Identify the preparation type.
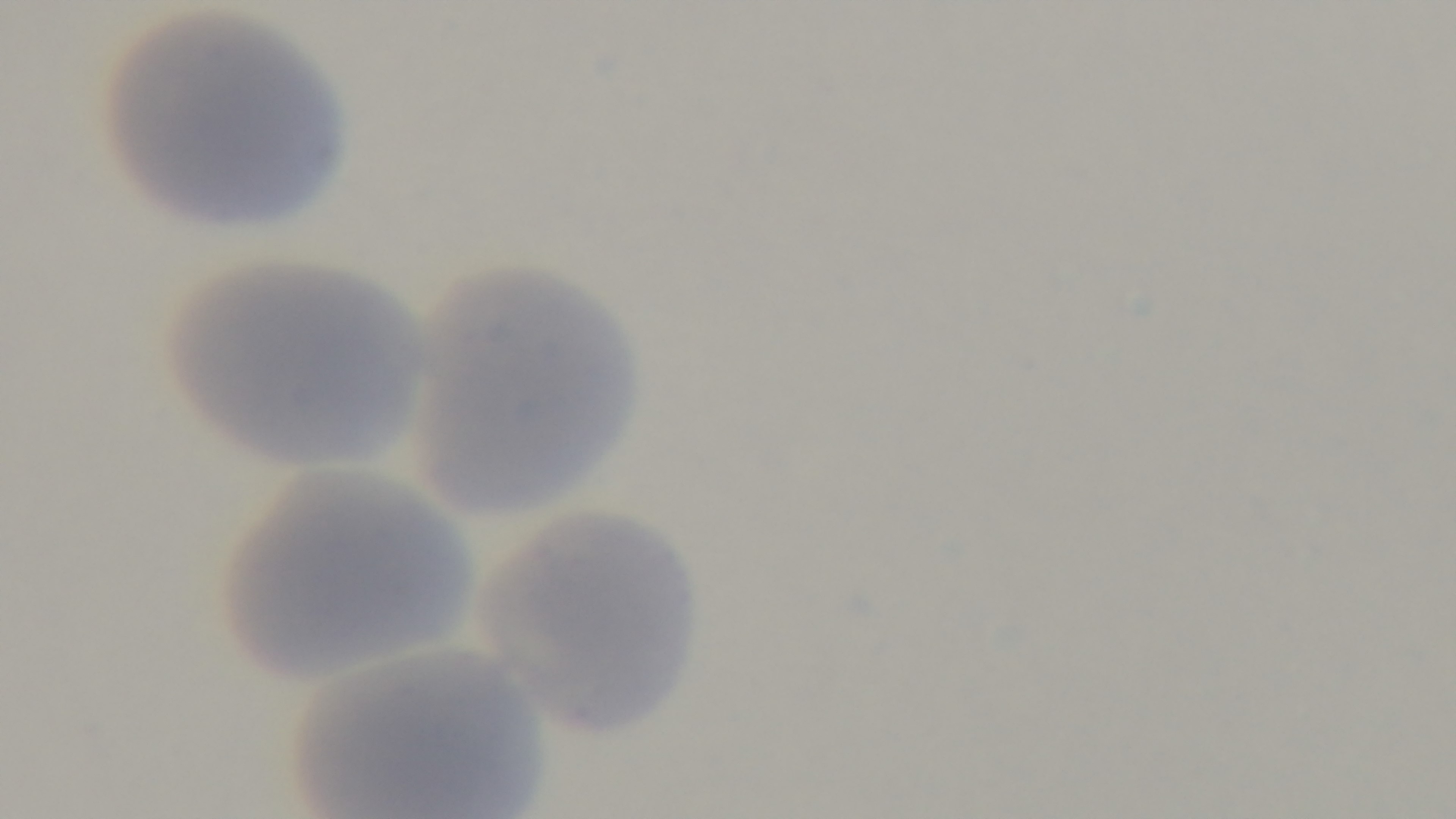

It is a thin blood film.

Summary:
  - Capture: mounted 4K digital camera
  - Stain: Giemsa
  - Malaria status: negative
  - Modality: light microscopy
  - Objective: 100x oil immersion
  - Field of view: single